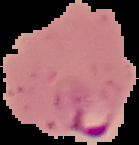
image size = 139×145 pixels
image type = segmented cell region on a black background
result = Plasmodium parasites detected
preparation = thin blood smear